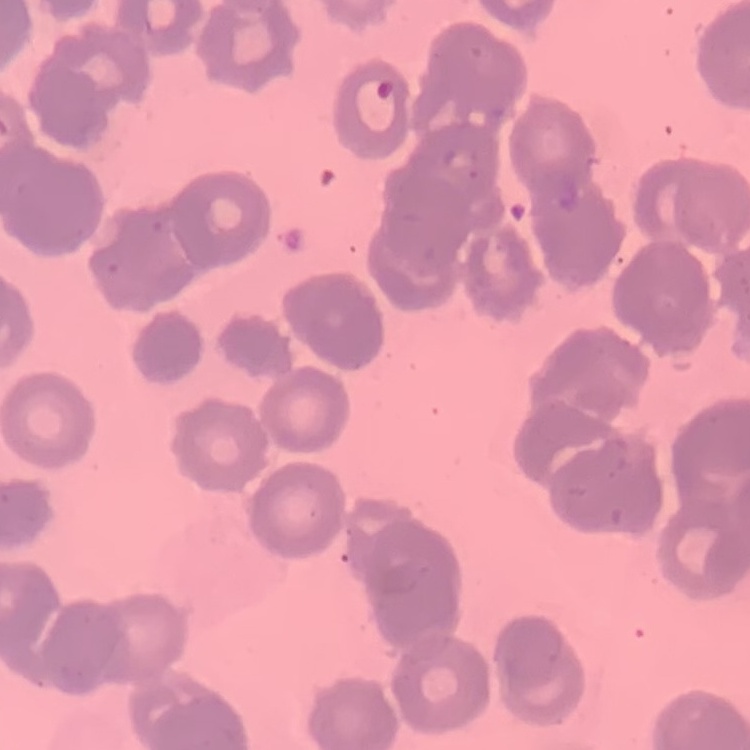 The erythrocytes show rouleaux formation. Stained with either Field's or Giemsa. Square crop of a larger photomicrograph. Thin blood film.